Classify this cell by malaria status.
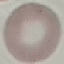

It is uninfected.

Thin blood film. Photographed with a smartphone camera at the microscope eyepiece. Automatically extracted cell patch, resized to 64 × 64 pixels. Giemsa stain.